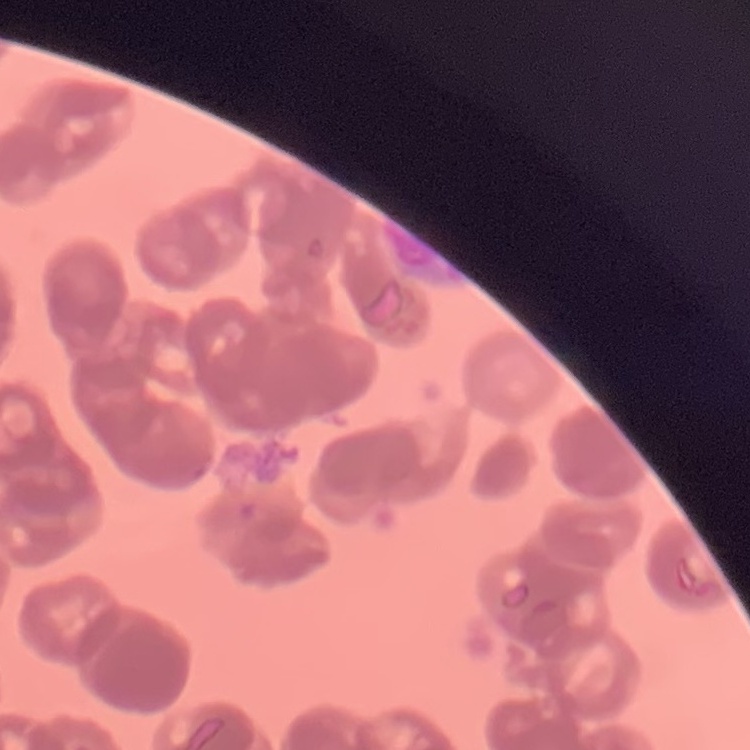

erythrocyte morphology = rouleaux formation
stain = Field's or Giemsa
preparation = thin blood smear
image type = square crop of a larger photomicrograph